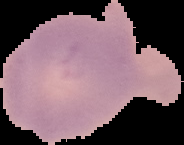
image size = 184×145 pixels
preparation = thin blood smear
malaria status = uninfected
image type = segmented cell region on a black background